Look for Plasmodium parasites.
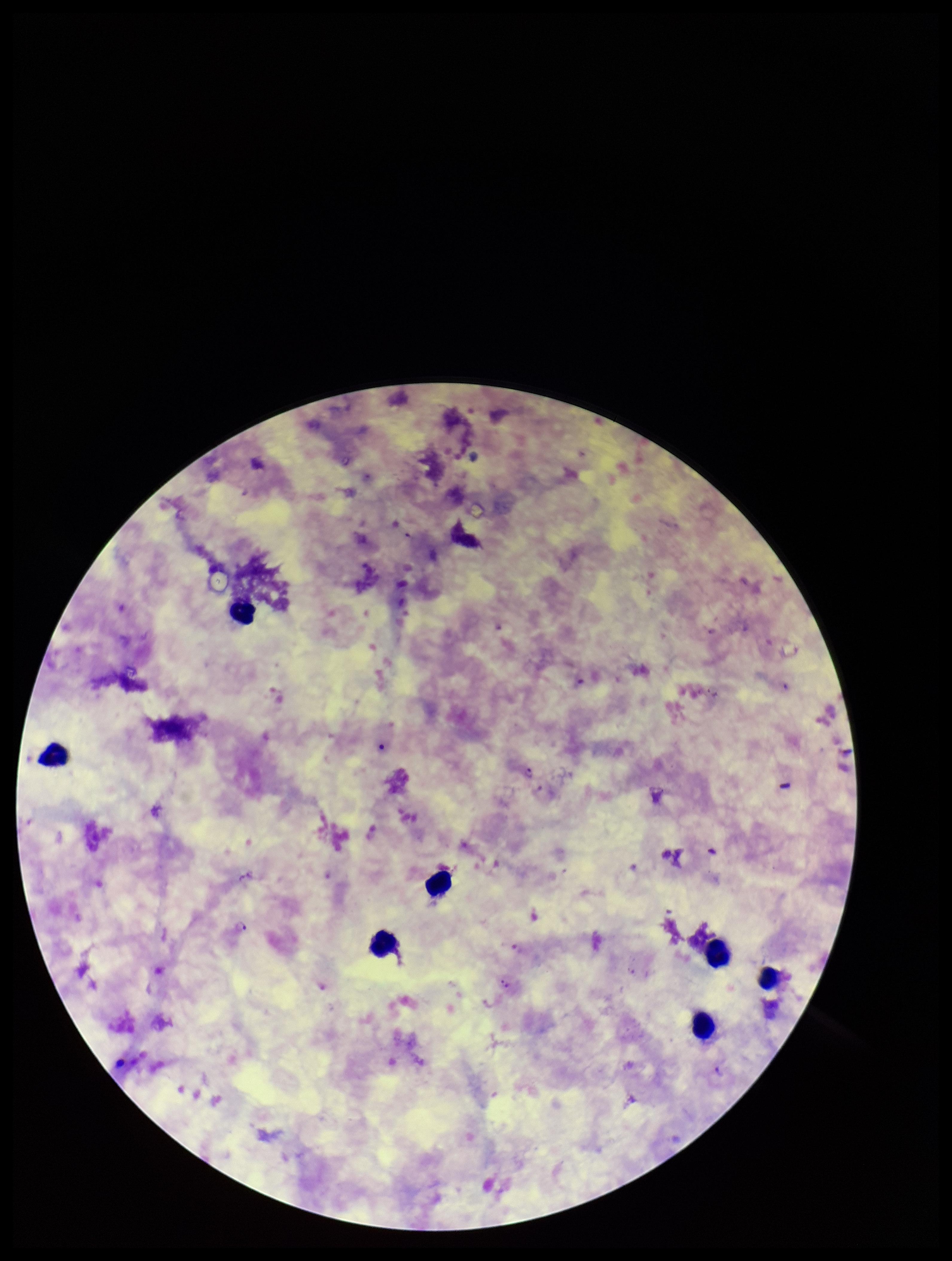
Identified.

Stained with Giemsa. Image is 952×1261 pixels. Parasite count: 4. Preparation: thick smear. Species reported for this patient: Plasmodium falciparum. One field from this slide. Leukocyte count: 7. Patient malaria status: infected. Photographed through the microscope eyepiece with a smartphone camera.